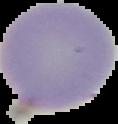 Result: no malaria parasites seen. Image is 118×124 pixels. From a thin blood smear. Cell region segmented out of the field of view; the surrounding area is masked to black.